Locate every blood parasite and identify its species.
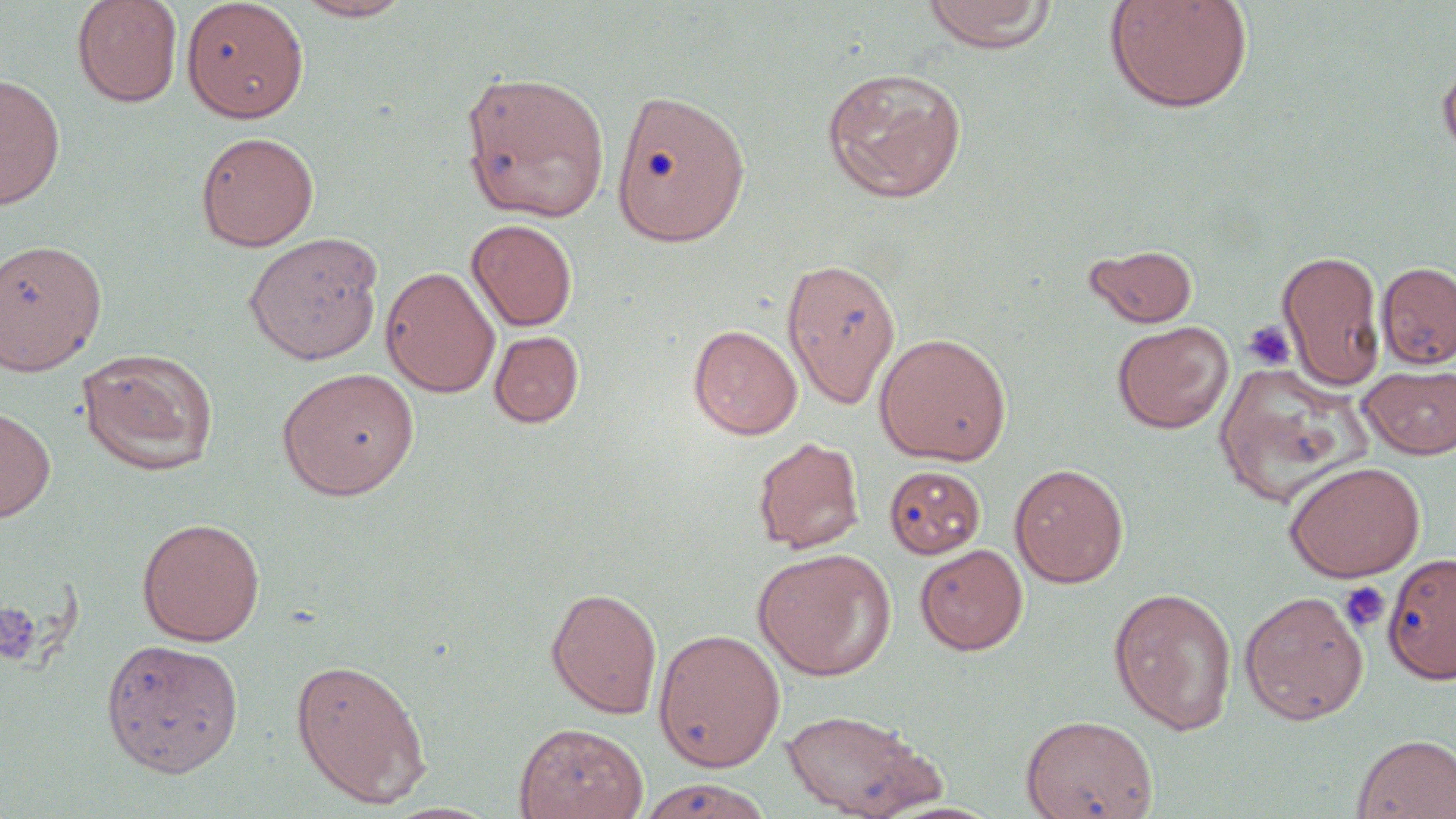
No blood parasites observed.

slide-level diagnosis = no evidence of blood parasites
preparation = thin blood smear
magnification = 1000x
stain = May-Grünwald-Giemsa
field of view = one of a larger specimen
image size = 1456×819 pixels
platelet locations = approximate bounding boxes as named x1/y1/x2/y2 corners in pixels: (x1=1242, y1=320, x2=1296, y2=370), (x1=1339, y1=581, x2=1391, y2=632), (x1=0, y1=601, x2=43, y2=666)
uninfected red blood cell locations = approximate bounding boxes as named x1/y1/x2/y2 corners in pixels: (x1=71, y1=0, x2=183, y2=107), (x1=181, y1=0, x2=310, y2=123), (x1=293, y1=0, x2=413, y2=22), (x1=921, y1=0, x2=1058, y2=53), (x1=1103, y1=0, x2=1255, y2=114), (x1=1438, y1=58, x2=1456, y2=162), (x1=821, y1=65, x2=968, y2=203), (x1=461, y1=71, x2=610, y2=221), (x1=0, y1=75, x2=66, y2=207), (x1=609, y1=88, x2=751, y2=247), (x1=195, y1=130, x2=319, y2=252), (x1=466, y1=219, x2=578, y2=331), (x1=243, y1=231, x2=384, y2=365), (x1=0, y1=238, x2=106, y2=375), (x1=1084, y1=243, x2=1198, y2=328), (x1=1277, y1=249, x2=1386, y2=390), (x1=781, y1=256, x2=902, y2=409), (x1=1376, y1=261, x2=1456, y2=369), (x1=381, y1=266, x2=500, y2=398), (x1=1112, y1=320, x2=1233, y2=434), (x1=687, y1=323, x2=802, y2=440), (x1=488, y1=330, x2=584, y2=428), (x1=874, y1=332, x2=1012, y2=465), (x1=77, y1=349, x2=219, y2=476), (x1=1359, y1=364, x2=1456, y2=459), (x1=276, y1=366, x2=420, y2=500), (x1=0, y1=405, x2=56, y2=523), (x1=752, y1=436, x2=864, y2=554), (x1=1283, y1=460, x2=1426, y2=582), (x1=1009, y1=463, x2=1128, y2=587), (x1=884, y1=465, x2=986, y2=559), (x1=136, y1=516, x2=265, y2=645), (x1=914, y1=543, x2=1028, y2=655), (x1=753, y1=548, x2=896, y2=681), (x1=1382, y1=552, x2=1456, y2=685), (x1=546, y1=586, x2=663, y2=718), (x1=1108, y1=586, x2=1237, y2=735), (x1=1239, y1=590, x2=1368, y2=725), (x1=652, y1=628, x2=785, y2=772), (x1=100, y1=638, x2=244, y2=777), (x1=290, y1=657, x2=432, y2=808), (x1=780, y1=707, x2=944, y2=819), (x1=1020, y1=713, x2=1158, y2=818), (x1=513, y1=722, x2=648, y2=819), (x1=1351, y1=733, x2=1456, y2=818), (x1=637, y1=777, x2=772, y2=819)
modality = optical microscopy